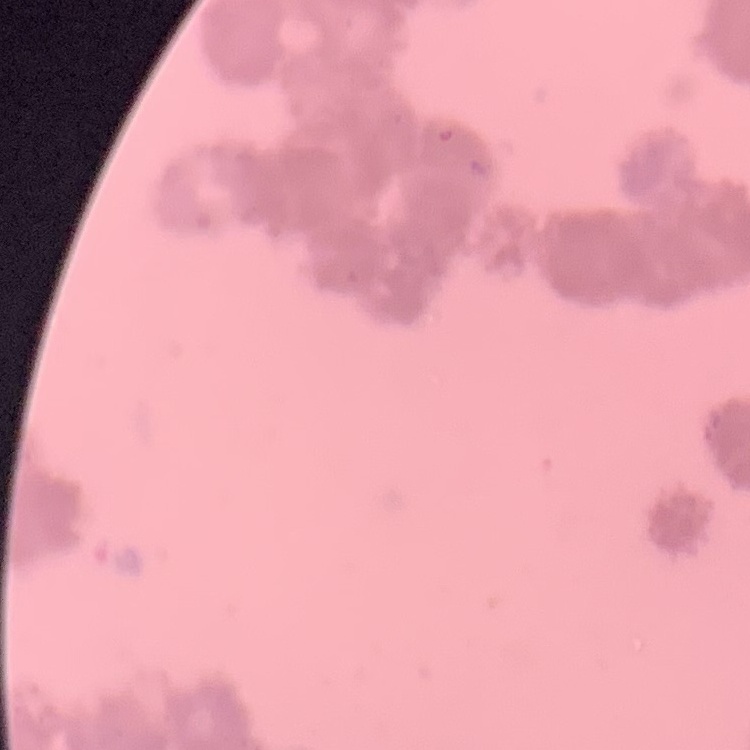

{
  "red_blood_cell_morphology": "rouleaux formation",
  "stain": "Field's or Giemsa",
  "preparation": "thin blood film",
  "image_type": "one tile cut from a larger photomicrograph"
}